Locate every Plasmodium falciparum-infected red blood cell.
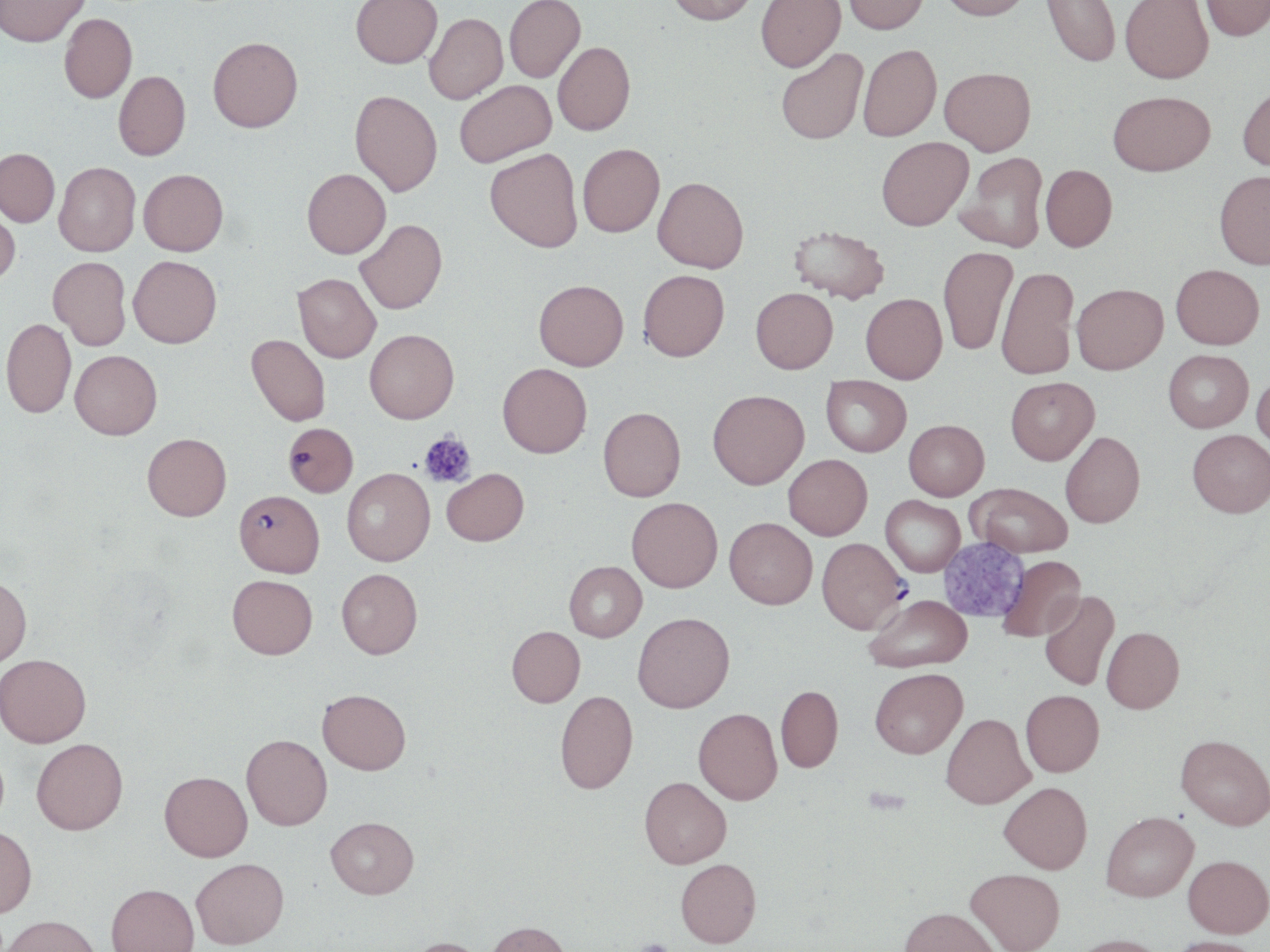
Approximate bounding boxes as [x1, y1, x2, y2] in pixels.
Plasmodium falciparum-infected red blood cells: [283, 422, 358, 497], [234, 489, 324, 576], [817, 537, 908, 634].

Summary:
  - Uninfected red blood cell locations: [0, 0, 91, 47], [350, 0, 442, 70], [504, 0, 585, 84], [666, 0, 758, 29], [757, 0, 846, 75], [843, 0, 929, 37], [938, 0, 1032, 24], [1040, 0, 1120, 69], [1120, 0, 1213, 87], [1200, 0, 1270, 44], [59, 13, 137, 104], [424, 15, 508, 106], [208, 37, 303, 133], [553, 44, 635, 138], [858, 46, 941, 143], [776, 50, 867, 146], [939, 68, 1036, 157], [114, 71, 191, 160], [455, 81, 556, 169], [1237, 86, 1270, 176], [349, 90, 442, 197], [1107, 91, 1215, 178], [877, 136, 973, 232], [578, 143, 665, 238], [0, 148, 60, 227], [485, 148, 583, 253], [956, 152, 1048, 253], [54, 162, 140, 256], [1041, 164, 1117, 252], [302, 168, 391, 258], [138, 169, 228, 256], [1215, 172, 1270, 271], [653, 176, 749, 273], [0, 204, 21, 286], [354, 219, 447, 314], [788, 224, 889, 303], [938, 246, 1017, 356], [129, 255, 221, 347], [48, 256, 131, 350], [1171, 264, 1264, 349], [996, 267, 1079, 380], [638, 269, 729, 362], [293, 273, 381, 362], [533, 279, 628, 370], [1071, 283, 1167, 374], [751, 287, 838, 373], [861, 293, 947, 383], [2, 318, 75, 417], [364, 328, 459, 422], [246, 334, 331, 425], [1163, 349, 1253, 432], [70, 350, 162, 439], [498, 363, 592, 458], [1252, 372, 1270, 455], [821, 376, 911, 456], [1006, 376, 1099, 464], [707, 389, 809, 488], [598, 406, 686, 501], [904, 419, 989, 500], [1188, 429, 1270, 517], [1060, 431, 1145, 528], [142, 433, 232, 520], [783, 454, 872, 540], [342, 468, 435, 566], [442, 468, 528, 546], [968, 483, 1072, 557], [881, 495, 965, 576], [626, 497, 722, 592], [724, 517, 817, 609], [999, 556, 1086, 641], [565, 561, 647, 642], [336, 567, 423, 658], [0, 575, 31, 667], [227, 575, 317, 659], [1039, 590, 1119, 690], [864, 593, 972, 672], [633, 612, 735, 712], [506, 626, 585, 707], [1101, 627, 1184, 713], [0, 653, 91, 746], [870, 667, 967, 758], [776, 684, 843, 773], [317, 689, 411, 774], [555, 690, 638, 794], [1021, 690, 1104, 777], [693, 707, 782, 805], [942, 712, 1035, 808], [1176, 733, 1270, 830], [241, 734, 332, 830], [32, 738, 128, 834], [160, 771, 253, 861], [639, 776, 732, 868], [999, 781, 1092, 874], [1101, 811, 1198, 901], [326, 816, 419, 898], [0, 825, 37, 917], [1183, 854, 1270, 937], [191, 857, 289, 948], [675, 858, 761, 947], [966, 868, 1065, 951], [106, 883, 199, 952], [898, 906, 1002, 952], [2, 914, 101, 952], [485, 921, 574, 952], [1069, 934, 1169, 952], [1168, 936, 1264, 952], [403, 937, 492, 952]
  - Platelet locations: [419, 430, 476, 489], [632, 937, 672, 951]
  - Slide-level diagnosis: Plasmodium falciparum
  - Field of view: single
  - Preparation: thin blood smear
  - Stain: May-Grünwald-Giemsa
  - Image size: 1270×952 pixels
  - Modality: light microscopy
  - Magnification: 1000x